Assess for malaria.
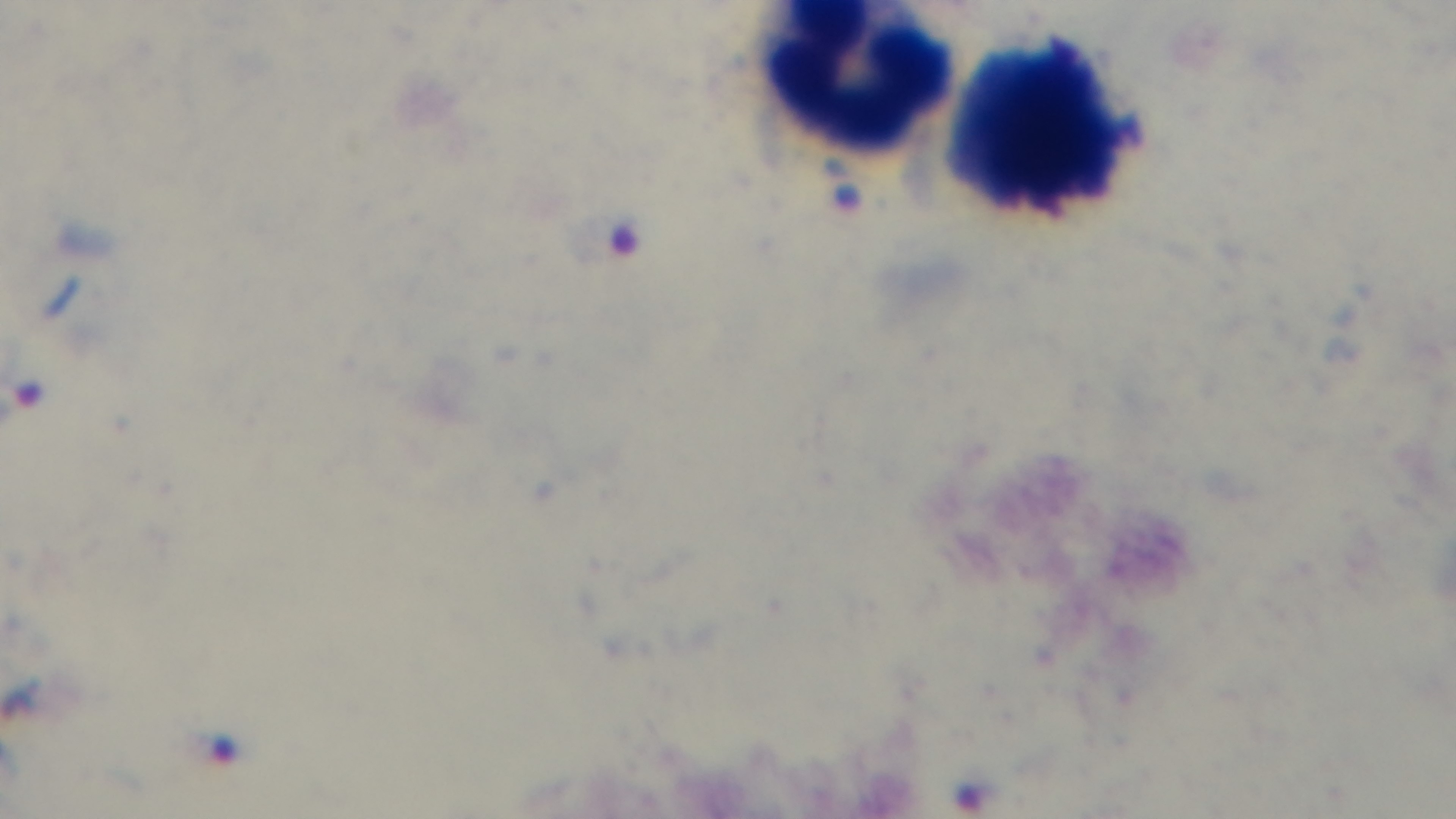

Infected.

Summary:
  - Objective: 100x oil immersion
  - Stain: Giemsa
  - Preparation: thick
  - Modality: light microscopy
  - Field of view: single
  - Capture: mounted 4K digital camera